Assess this cell for malaria.
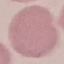
Uninfected.

Giemsa-stained preparation. Cell patch, automatically extracted from a larger field of view and resized to 64 × 64 pixels. Thin blood smear. Photographed with a smartphone camera at the microscope eyepiece.